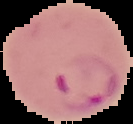

Malaria status: parasitized. From a thin blood smear. Image is 133×124 pixels. Segmented cell region on a black background.